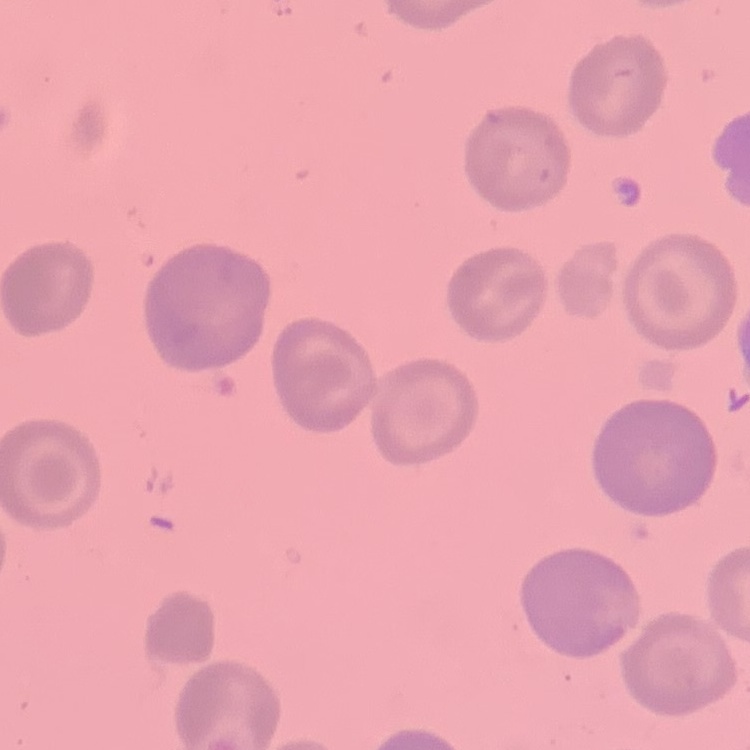
The erythrocytes show no rouleaux formation. Square crop of a larger photomicrograph. Thin blood film. Field's or Giemsa stain.